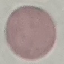
Summary:
  - Result: no malaria parasites seen
  - Stain: Giemsa
  - Preparation: thin blood smear
  - Image type: automatically extracted cell patch, resized to 64 × 64 pixels
  - Capture: smartphone camera at the microscope eyepiece